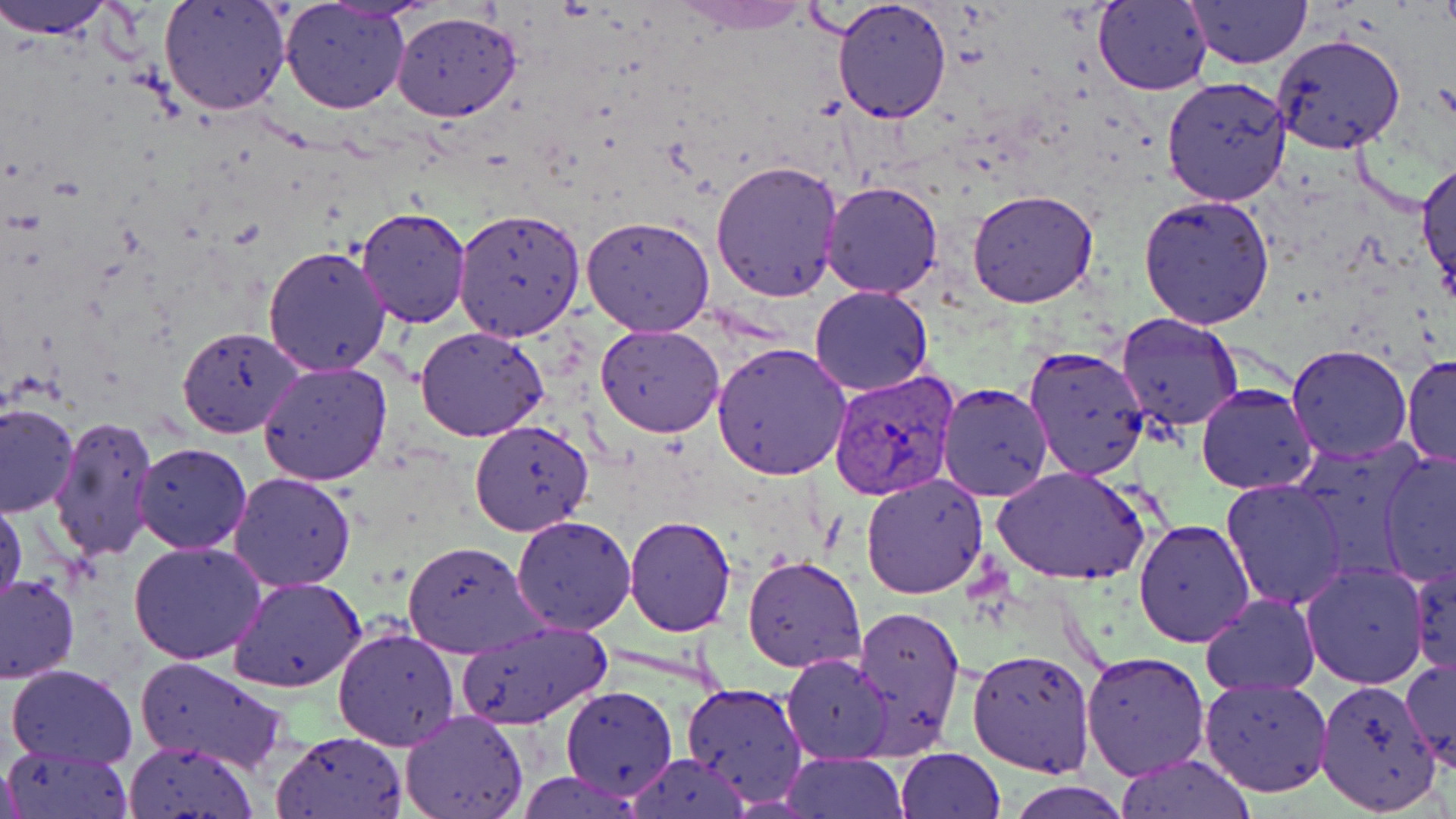

slide_level_diagnosis: Plasmodium vivax
preparation: thin blood film
magnification: 1000x
plasmodium_vivax_infected_red_blood_cell_locations: 'approximate bounding boxes as (x1, y1, x2, y2) in pixels: (828, 369, 957, 500)'
uninfected_red_blood_cell_locations: 'approximate bounding boxes as (x1, y1, x2, y2) in pixels: (0, 0, 119, 40), (158, 0, 292, 118), (320, 0, 436, 23), (831, 0, 952, 124), (280, 1, 412, 116), (1185, 1, 1312, 70), (672, 2, 812, 35), (1093, 2, 1212, 95), (391, 11, 521, 122), (1270, 33, 1407, 155), (1162, 77, 1294, 206), (1416, 157, 1456, 299), (711, 161, 844, 305), (819, 179, 945, 299), (967, 189, 1098, 309), (1138, 192, 1275, 328), (354, 208, 473, 329), (453, 208, 586, 342), (581, 214, 716, 337), (262, 244, 393, 378), (808, 285, 935, 396), (1114, 309, 1243, 433), (596, 323, 726, 437), (177, 326, 307, 438), (414, 326, 550, 441), (221, 336, 361, 458), (711, 343, 853, 480), (1287, 345, 1412, 463), (1023, 347, 1150, 482), (1403, 354, 1456, 472), (257, 361, 391, 486), (936, 382, 1054, 501), (1195, 382, 1320, 495), (0, 402, 79, 516), (49, 416, 159, 564), (469, 419, 595, 536), (1289, 433, 1431, 579), (132, 442, 252, 553), (1377, 450, 1456, 588), (993, 466, 1150, 586), (227, 471, 357, 592), (861, 474, 989, 599), (1221, 478, 1348, 610), (0, 490, 24, 615), (511, 516, 637, 635), (623, 516, 737, 636), (1134, 519, 1255, 646), (403, 540, 543, 659), (129, 541, 266, 664), (742, 555, 866, 674), (1407, 557, 1455, 678), (1301, 565, 1428, 689), (1, 574, 79, 684), (229, 575, 368, 692), (1200, 593, 1321, 696), (848, 605, 965, 757), (455, 621, 612, 727), (332, 625, 461, 751), (968, 647, 1096, 777), (1080, 649, 1211, 779), (781, 654, 893, 763), (1401, 655, 1455, 770), (134, 657, 291, 773), (6, 664, 137, 768), (1199, 677, 1333, 797), (1313, 679, 1443, 817), (681, 682, 808, 808), (559, 684, 677, 800), (400, 709, 529, 819), (272, 730, 407, 818), (123, 741, 257, 818), (4, 746, 135, 819), (895, 748, 1005, 818), (782, 752, 909, 818), (626, 753, 751, 819), (1116, 754, 1256, 818), (0, 756, 27, 817), (516, 770, 644, 817), (1006, 780, 1133, 819)'
stain: May-Grünwald-Giemsa
modality: light microscopy
image_size: 1456×819 pixels
field_of_view: one of a larger specimen